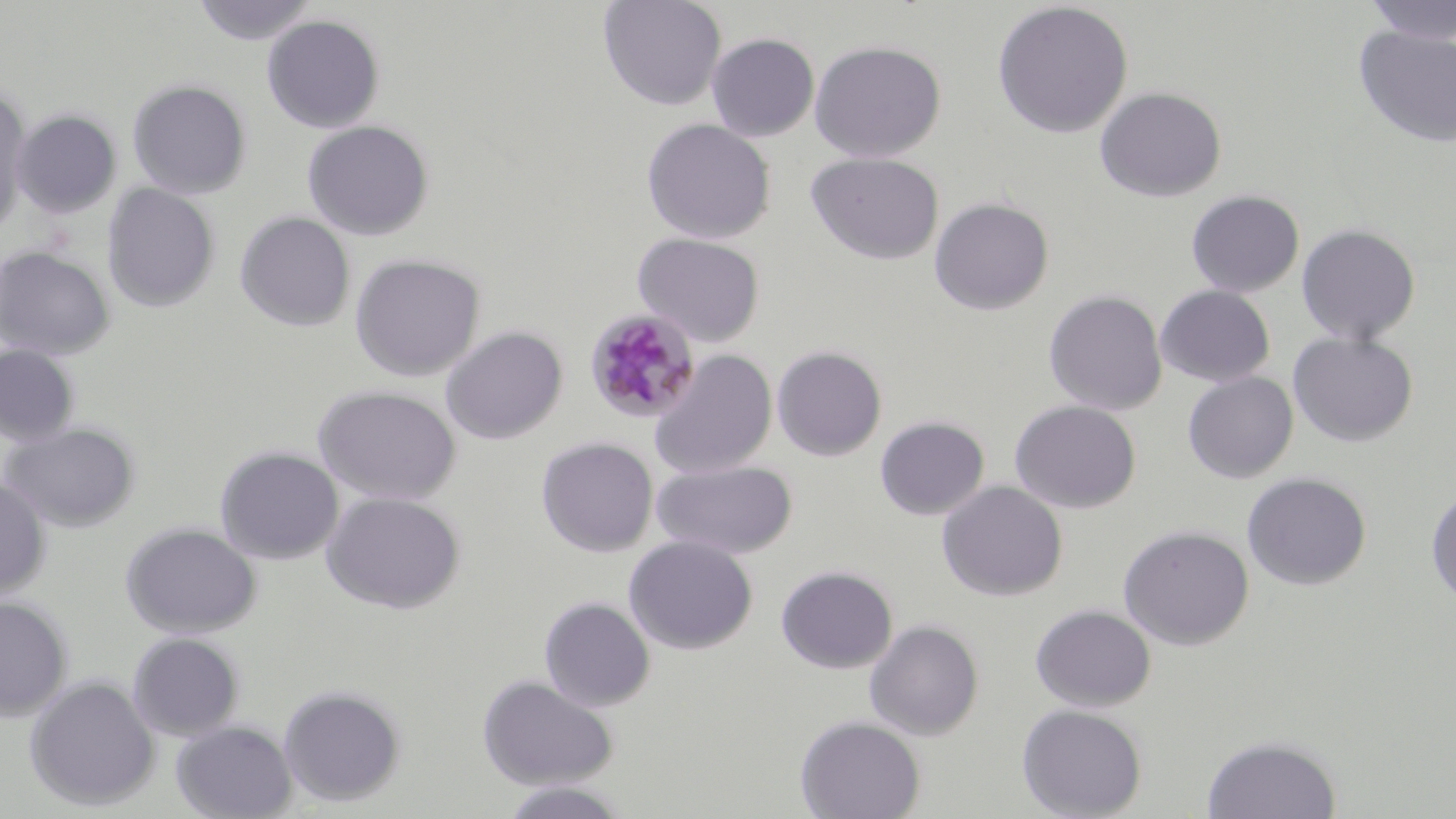
Approximate bounding boxes as (x1,y1)-(x2,y2) corner pairs in pixels. Uninfected red blood cell locations: (190,0)-(318,45), (597,0)-(727,111), (1361,0)-(1456,44), (991,2)-(1133,139), (262,14)-(385,133), (1352,25)-(1456,148), (706,33)-(820,141), (808,40)-(946,162), (127,79)-(252,199), (1094,86)-(1227,202), (0,89)-(31,234), (11,110)-(122,218), (640,118)-(776,244), (302,121)-(434,241), (805,151)-(944,265), (102,183)-(220,313), (1186,190)-(1304,298), (929,197)-(1054,315), (236,212)-(355,331), (1296,223)-(1421,345), (632,232)-(766,347), (0,245)-(115,360), (350,253)-(485,382), (1155,285)-(1275,387), (1044,289)-(1168,415), (441,326)-(568,444), (1288,332)-(1419,447), (0,344)-(81,447), (772,345)-(887,461), (648,349)-(777,478), (1183,371)-(1299,484), (313,385)-(461,505), (1009,400)-(1141,514), (875,416)-(989,521), (2,422)-(141,532), (537,437)-(658,557), (215,446)-(344,565), (652,459)-(798,560), (1242,472)-(1372,590), (0,478)-(51,600), (936,481)-(1067,601), (1425,486)-(1456,607), (322,491)-(466,614), (120,522)-(262,638), (1117,524)-(1255,650), (624,536)-(758,654), (776,565)-(897,674), (0,595)-(73,721), (539,597)-(655,712), (1030,603)-(1156,712), (864,620)-(984,740), (127,632)-(244,740), (477,674)-(619,790), (24,676)-(160,811), (278,683)-(407,807), (1016,704)-(1148,819), (795,715)-(926,819), (171,721)-(296,819), (1201,734)-(1342,818), (499,780)-(632,819). Plasmodium malariae-infected red blood cell locations: (584,308)-(701,425). Slide-level diagnosis: Plasmodium malariae. Captured at 1000x magnification. Optical microscopy. Image is 1456×819 pixels. Thin blood film. May-Grünwald-Giemsa stain. One field of a larger specimen.